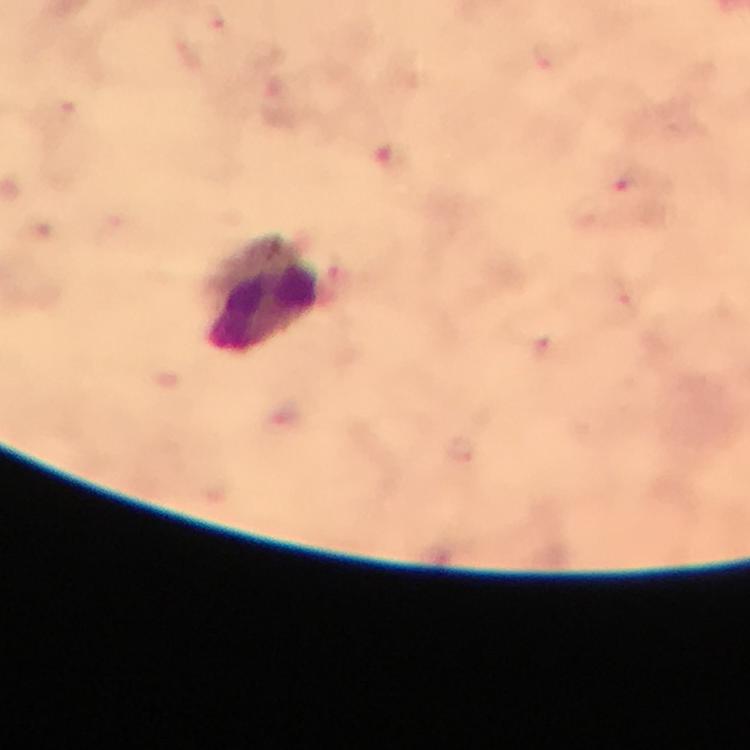

image size = 750×750 pixels
magnification = 100x
Plasmodium parasite locations = approximate centers as [x, y] in pixels: [215, 20], [546, 56], [629, 181], [543, 345], [461, 448]
cropped from = one field of view
leukocyte locations = approximate centers as [x, y] in pixels: [265, 298]
stain = Giemsa
immersion oil = applied
preparation = thick blood smear
capture = smartphone photograph through a microscope
context = from a malaria diagnostic workup